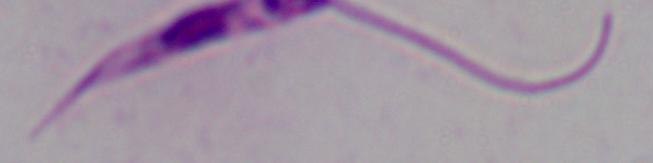

identification = Leishmania
modality = micrograph
magnification = 1000x